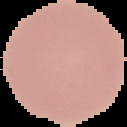

{
  "result": "no Plasmodium parasites seen",
  "image_type": "segmented cell region with the area outside set to black",
  "preparation": "thin blood film",
  "image_size": "127×127 pixels"
}